Assess this cell for malaria.
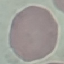
It is uninfected.

Summary:
  - Image type: cell patch, automatically extracted from a larger field of view and resized to 64 × 64 pixels
  - Capture: smartphone camera at the microscope eyepiece
  - Preparation: thin smear
  - Stain: Giemsa